Locate platelets.
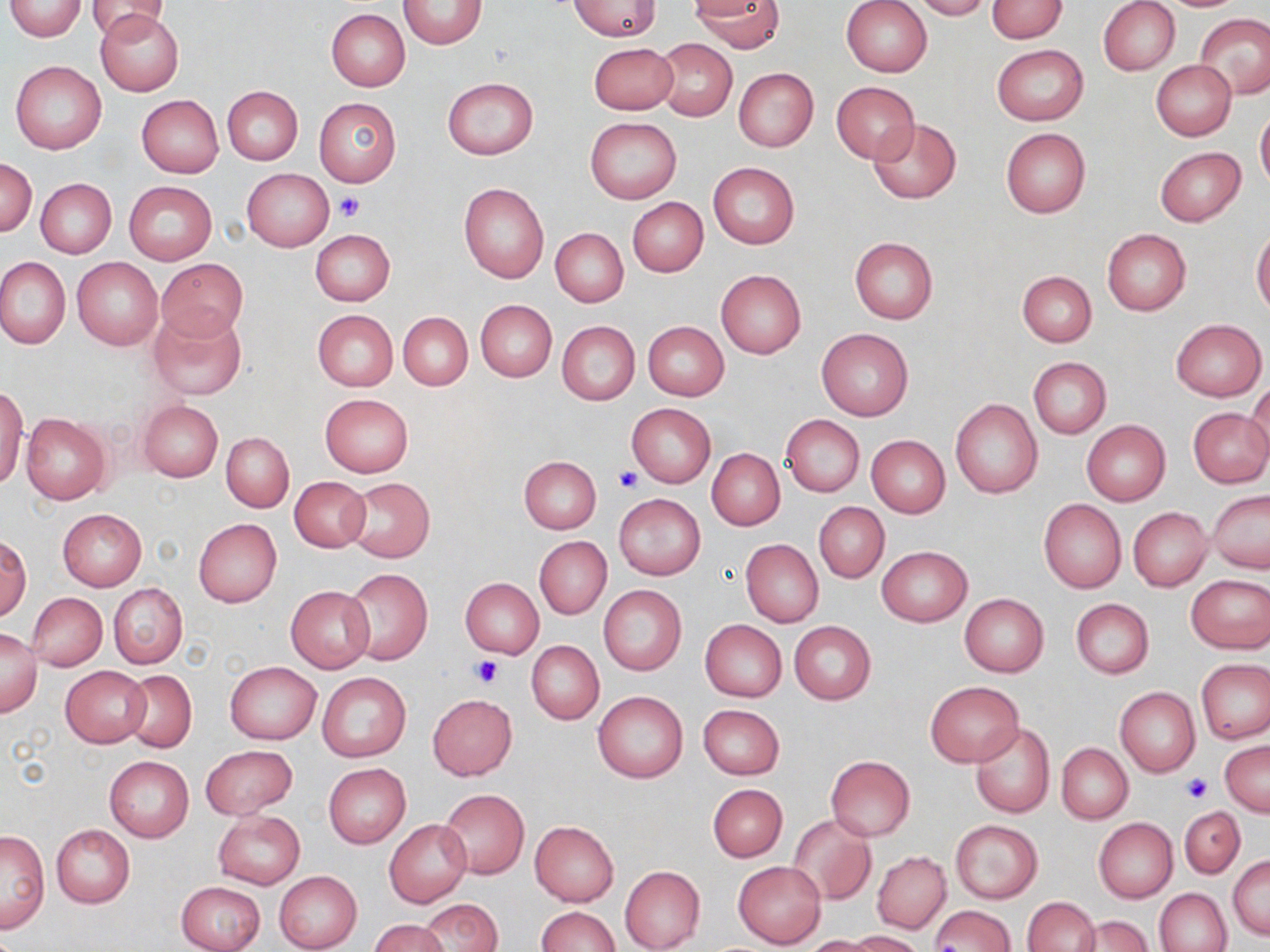
Approximate bounding boxes as [x1, y1, x2, y2] in pixels.
Platelets: [335, 192, 366, 222], [616, 466, 644, 493], [470, 654, 504, 687], [1182, 774, 1210, 802].

Summary:
  - Uninfected red blood cell locations: [85, 0, 173, 40], [841, 0, 933, 77], [912, 0, 990, 19], [986, 0, 1067, 41], [1098, 0, 1180, 76], [5, 1, 88, 41], [398, 1, 486, 49], [692, 1, 782, 53], [569, 2, 662, 40], [327, 9, 409, 92], [96, 10, 184, 96], [1195, 13, 1270, 99], [653, 39, 737, 120], [590, 42, 677, 114], [992, 45, 1088, 125], [10, 59, 107, 154], [1151, 60, 1237, 140], [733, 67, 819, 152], [441, 77, 538, 161], [831, 82, 921, 163], [222, 86, 302, 164], [136, 95, 223, 177], [313, 96, 402, 188], [1256, 108, 1270, 191], [587, 118, 682, 202], [868, 118, 962, 203], [1001, 128, 1090, 217], [1154, 147, 1247, 226], [2, 158, 37, 236], [708, 162, 800, 249], [242, 169, 333, 251], [36, 179, 115, 257], [124, 181, 217, 263], [459, 182, 550, 284], [627, 197, 708, 277], [551, 228, 629, 307], [310, 229, 395, 305], [1102, 229, 1191, 315], [1252, 229, 1270, 315], [849, 237, 938, 324], [0, 256, 70, 350], [72, 257, 163, 351], [157, 259, 248, 340], [715, 270, 807, 358], [1017, 270, 1096, 346], [475, 299, 556, 382], [147, 304, 247, 400], [312, 309, 397, 392], [398, 312, 472, 389], [1171, 319, 1266, 400], [558, 321, 639, 405], [643, 321, 729, 400], [815, 327, 914, 421], [1027, 357, 1109, 438], [1244, 379, 1270, 463], [0, 384, 28, 490], [320, 393, 413, 477], [950, 399, 1042, 498], [137, 400, 223, 481], [626, 403, 715, 488], [1187, 408, 1269, 488], [21, 413, 111, 504], [781, 415, 865, 497], [1081, 420, 1170, 505], [221, 431, 294, 512], [866, 435, 950, 516], [707, 448, 785, 531], [518, 456, 601, 534], [290, 475, 369, 552], [345, 478, 434, 562], [1207, 491, 1269, 573], [614, 493, 706, 580], [1038, 498, 1126, 593], [815, 503, 889, 583], [1128, 507, 1212, 591], [58, 508, 147, 590], [193, 518, 282, 608], [534, 535, 611, 619], [2, 536, 31, 620], [741, 540, 823, 627], [877, 546, 972, 627], [344, 569, 432, 666], [1185, 575, 1270, 654], [460, 577, 544, 658], [108, 582, 187, 669], [599, 585, 686, 675], [285, 587, 374, 672], [28, 593, 106, 671], [959, 593, 1049, 676], [1071, 598, 1154, 679], [699, 620, 786, 702], [789, 621, 876, 704], [0, 628, 41, 717], [528, 641, 604, 723], [1197, 659, 1269, 744], [225, 661, 321, 743], [61, 665, 150, 748], [121, 670, 196, 753], [317, 672, 411, 763], [924, 681, 1024, 767], [1115, 687, 1200, 776], [592, 689, 688, 783], [427, 693, 517, 780], [697, 704, 785, 779], [970, 722, 1055, 818], [1220, 741, 1270, 815], [1057, 743, 1132, 823], [201, 744, 297, 819], [825, 755, 915, 841], [104, 756, 194, 841], [323, 763, 411, 848], [708, 784, 787, 861], [439, 789, 530, 879], [1179, 805, 1245, 878], [213, 811, 304, 890], [788, 815, 877, 905], [385, 818, 472, 908], [950, 819, 1043, 904], [1094, 819, 1177, 901], [530, 820, 619, 906], [50, 824, 134, 908], [1, 828, 49, 933], [872, 851, 951, 933], [1229, 855, 1270, 940], [734, 861, 825, 948], [620, 866, 705, 951], [274, 871, 363, 952], [177, 881, 266, 952], [1156, 888, 1232, 952], [1022, 896, 1099, 952], [420, 899, 501, 951], [930, 905, 1014, 952], [535, 906, 619, 952], [1073, 914, 1152, 952], [370, 918, 449, 952], [847, 930, 925, 951], [802, 936, 880, 951]
  - Slide-level diagnosis: no evidence of blood parasites
  - Magnification: 1000x
  - Modality: light microscopy
  - Stain: May-Grünwald-Giemsa
  - Image size: 1270×952 pixels
  - Field of view: one of a larger specimen
  - Preparation: thin blood film